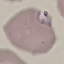 Malaria status: parasitized. Acquired by smartphone through the microscope eyepiece. Giemsa stain. Automatically extracted cell patch, resized to 64 × 64 pixels. Thin smear of blood.